Assess this cell for malaria.
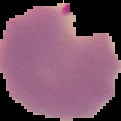
Parasitized.

From a thin blood film. Image is 121×121 pixels. The area outside the segmented cell region is set to black.